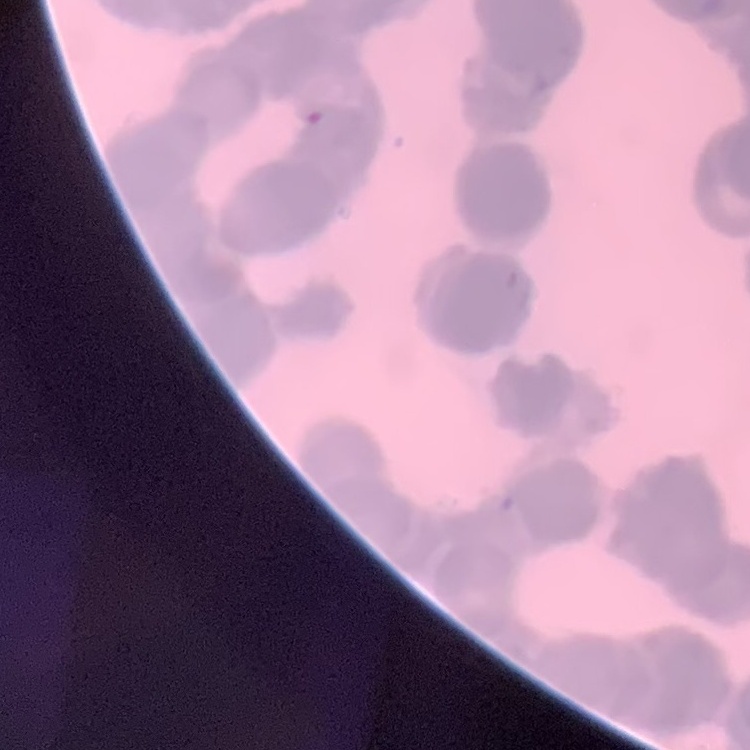 The erythrocytes exhibit rouleaux formation. One tile cut from a larger photomicrograph. Thin peripheral smear. Field's or Giemsa stain.